Assess this cell for malaria.
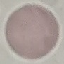
Uninfected.

Thin blood film. Acquired by smartphone through the microscope eyepiece. Automatically extracted cell patch, resized to 64 × 64 pixels. Giemsa-stained preparation.